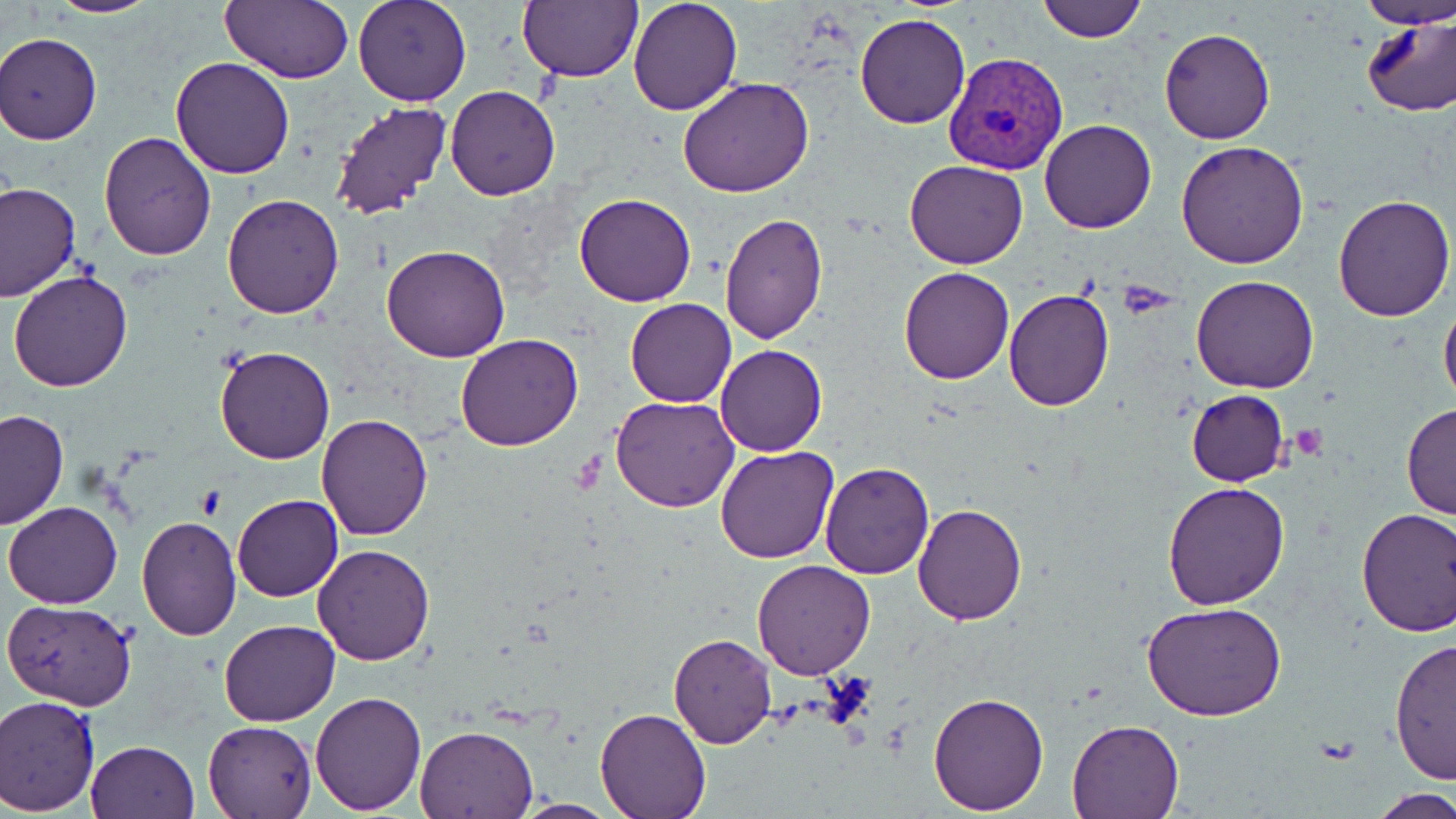

Approximate bounding boxes as (x1, y1, x2, y2) in pixels. Uninfected red blood cell locations: (44, 0, 162, 18), (221, 0, 352, 84), (352, 0, 471, 106), (629, 0, 743, 115), (1038, 0, 1148, 41), (1357, 0, 1455, 29), (516, 1, 641, 84), (855, 12, 971, 129), (1359, 13, 1455, 118), (1159, 27, 1275, 145), (0, 31, 103, 145), (169, 56, 296, 178), (678, 76, 814, 198), (446, 85, 561, 200), (329, 101, 450, 221), (1040, 120, 1156, 233), (98, 133, 217, 261), (1177, 139, 1310, 269), (905, 159, 1030, 270), (0, 181, 80, 302), (575, 192, 697, 308), (222, 193, 346, 319), (1331, 193, 1455, 321), (718, 212, 827, 343), (382, 245, 511, 364), (899, 267, 1014, 383), (7, 269, 133, 392), (1191, 275, 1319, 394), (1004, 286, 1115, 411), (1439, 294, 1456, 413), (624, 297, 736, 408), (455, 333, 583, 451), (716, 344, 827, 457), (214, 346, 336, 464), (1185, 389, 1290, 487), (611, 394, 741, 512), (1401, 402, 1456, 520), (0, 409, 68, 529), (314, 413, 433, 540), (715, 446, 839, 564), (820, 460, 934, 578), (1162, 481, 1290, 609), (232, 495, 342, 602), (3, 501, 123, 609), (912, 501, 1028, 624), (1355, 508, 1456, 637), (135, 517, 242, 639), (312, 543, 435, 666), (752, 560, 875, 679), (3, 598, 135, 708), (1141, 600, 1287, 721), (218, 618, 340, 726), (668, 633, 777, 748), (1389, 639, 1456, 783), (311, 689, 426, 813), (928, 691, 1049, 813), (1, 694, 101, 814), (594, 709, 711, 819), (202, 717, 317, 819), (1066, 718, 1185, 818), (415, 724, 541, 819), (84, 740, 200, 819), (1370, 790, 1455, 817). Plasmodium vivax-infected red blood cell locations: (943, 51, 1071, 176). Slide-level diagnosis: Plasmodium vivax. Captured at 1000x magnification. Single field of view. Image is 1456×819 pixels. Optical microscopy. Thin blood film. May-Grünwald-Giemsa stain.